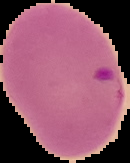

{
  "image_type": "segmented cell region on a black background",
  "image_size": "130×163 pixels",
  "malaria_status": "parasitized",
  "preparation": "thin blood film"
}